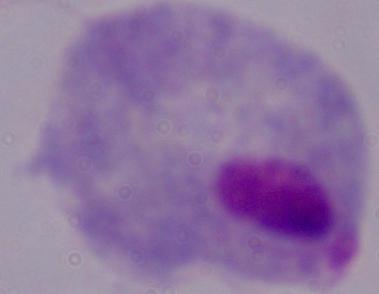 Micrograph. A trichomonad is seen. Captured at 1000x magnification.